Point out each leukocyte.
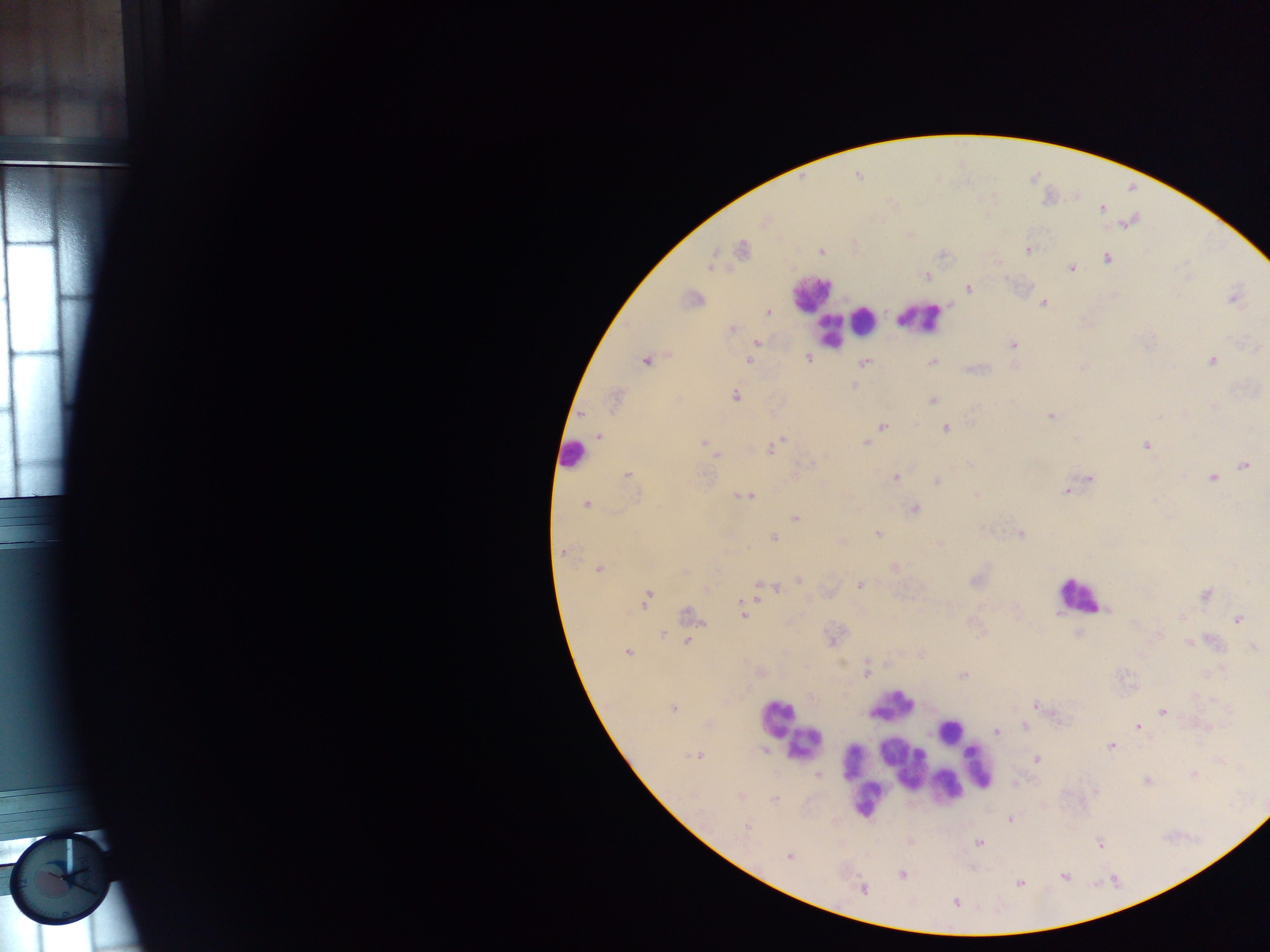

Approximate centers as {x, y} in pixels.
Leukocytes: {812, 293}, {920, 317}, {864, 319}, {830, 333}, {572, 454}, {1078, 595}, {894, 705}, {776, 718}, {949, 731}, {807, 742}, {854, 761}, {901, 761}, {978, 768}, {948, 785}, {866, 798}.

Summary:
  - Plasmodium parasite locations: {1102, 208}, {742, 249}, {1028, 250}, {822, 252}, {1108, 259}, {710, 266}, {1071, 268}, {924, 276}, {969, 288}, {1234, 298}, {693, 299}, {1044, 303}, {769, 313}, {732, 330}, {757, 342}, {1013, 344}, {752, 356}, {808, 358}, {749, 361}, {1212, 361}, {645, 362}, {933, 362}, {865, 363}, {1084, 367}, {854, 385}, {735, 397}, {614, 400}, {933, 400}, {1213, 406}, {1050, 416}, {882, 426}, {946, 429}, {599, 436}, {782, 440}, {703, 443}, {866, 443}, {1146, 445}, {772, 448}, {717, 456}, {970, 464}, {1245, 465}, {628, 474}, {895, 478}, {1212, 478}, {1089, 479}, {937, 482}, {1065, 491}, {977, 494}, {747, 496}, {586, 505}, {916, 509}, {795, 518}, {877, 533}, {1020, 533}, {774, 537}, {939, 543}, {564, 552}, {893, 568}, {598, 569}, {684, 571}, {798, 580}, {975, 580}, {860, 585}, {759, 586}, {776, 589}, {1205, 594}, {648, 597}, {742, 605}, {687, 612}, {742, 613}, {1237, 620}, {663, 634}, {832, 640}, {687, 641}, {1189, 644}, {1253, 648}, {627, 651}, {866, 672}, {964, 675}, {1035, 705}, {673, 708}, {1163, 712}, {1025, 725}, {1138, 726}, {997, 731}, {1111, 746}, {766, 750}, {697, 756}, {1037, 760}, {819, 775}, {1194, 775}, {1146, 780}, {741, 796}, {774, 800}, {1011, 819}, {746, 826}, {980, 842}, {1099, 843}, {789, 857}, {901, 874}, {1020, 882}, {862, 889}, {955, 903}
  - Field of view: single
  - Preparation: thick blood film
  - Image size: 1270×952 pixels
  - Country: Ghana
  - Capture: mobile-phone photograph through a microscope